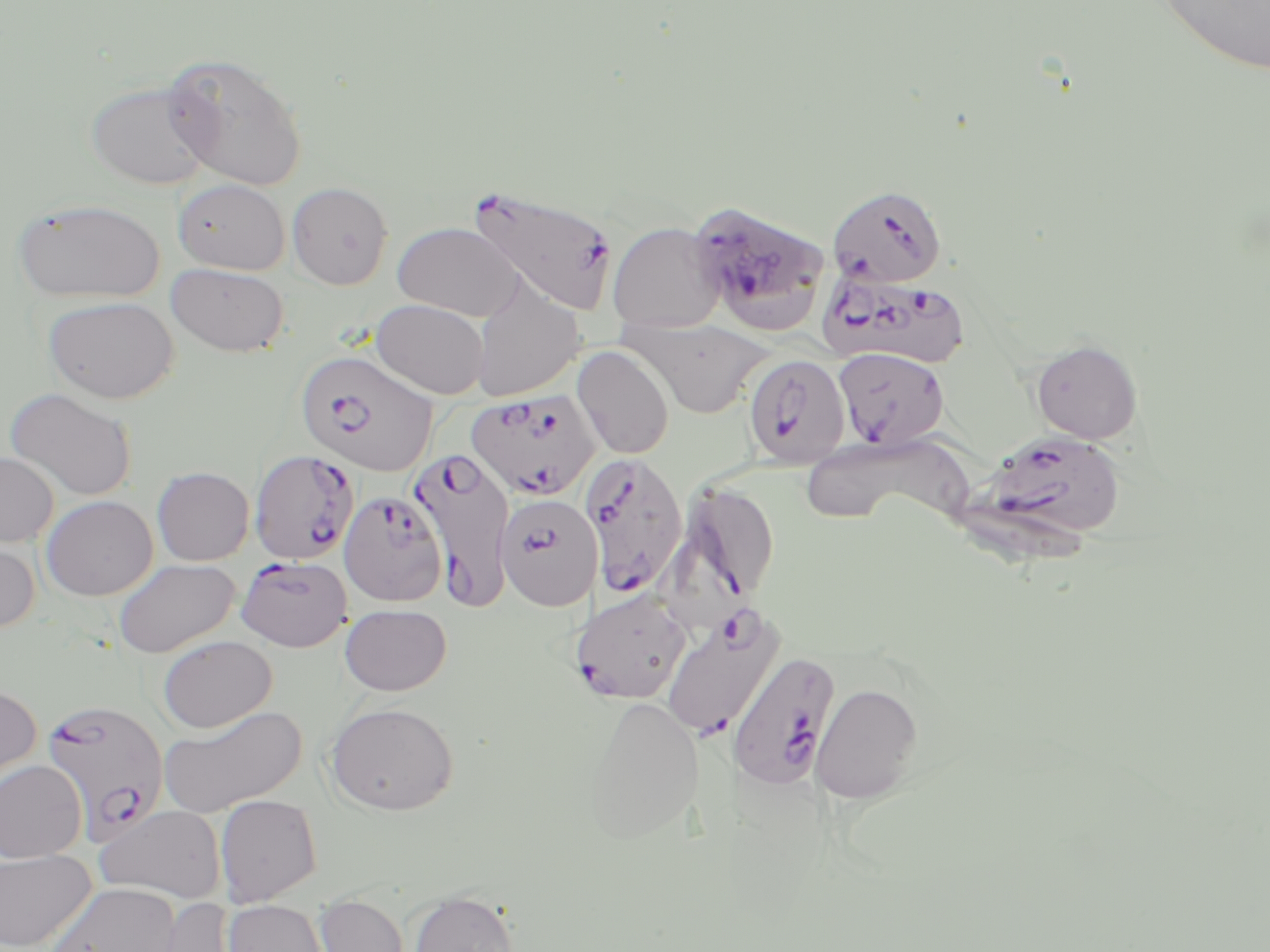 Approximate bounding boxes as (x1,y1)-(x2,y2) corner pairs in pixels. Uninfected red blood cell locations: (1155,0)-(1270,77), (161,52)-(309,191), (86,80)-(215,190), (173,178)-(290,275), (287,182)-(393,289), (11,197)-(165,303), (607,221)-(726,333), (392,222)-(523,321), (166,263)-(289,357), (469,278)-(585,402), (43,296)-(180,403), (372,299)-(489,398), (624,318)-(774,418), (1031,339)-(1142,444), (572,346)-(674,460), (4,387)-(137,502), (802,434)-(970,526), (0,452)-(58,547), (152,466)-(254,565), (41,495)-(158,600), (0,536)-(40,635), (113,558)-(240,657), (340,604)-(451,695), (157,635)-(277,733), (0,683)-(42,792), (811,683)-(924,804), (583,694)-(704,845), (325,702)-(459,815), (159,705)-(306,816), (0,759)-(87,862), (215,794)-(323,906), (94,804)-(227,903), (0,848)-(96,951), (46,883)-(180,952), (408,888)-(519,952), (315,893)-(409,952), (149,897)-(242,952), (224,900)-(327,952). Plasmodium falciparum-infected red blood cell locations: (467,184)-(619,319), (827,185)-(947,288), (688,199)-(830,331), (821,270)-(971,367), (834,347)-(950,449), (296,349)-(438,477), (746,356)-(855,472), (465,388)-(601,501), (985,431)-(1125,539), (409,447)-(516,610), (249,449)-(359,563), (580,451)-(689,600), (672,480)-(781,610), (338,490)-(448,606), (495,492)-(603,610), (236,556)-(353,651), (570,589)-(692,704), (660,606)-(785,739), (727,651)-(841,790), (41,699)-(169,843). Slide-level diagnosis: Plasmodium falciparum. Optical microscopy. Thin blood film. Image is 1270×952 pixels. May-Grünwald-Giemsa-stained preparation. One field of a larger specimen. 1000x magnification.